Assess the morphology of the erythrocytes.
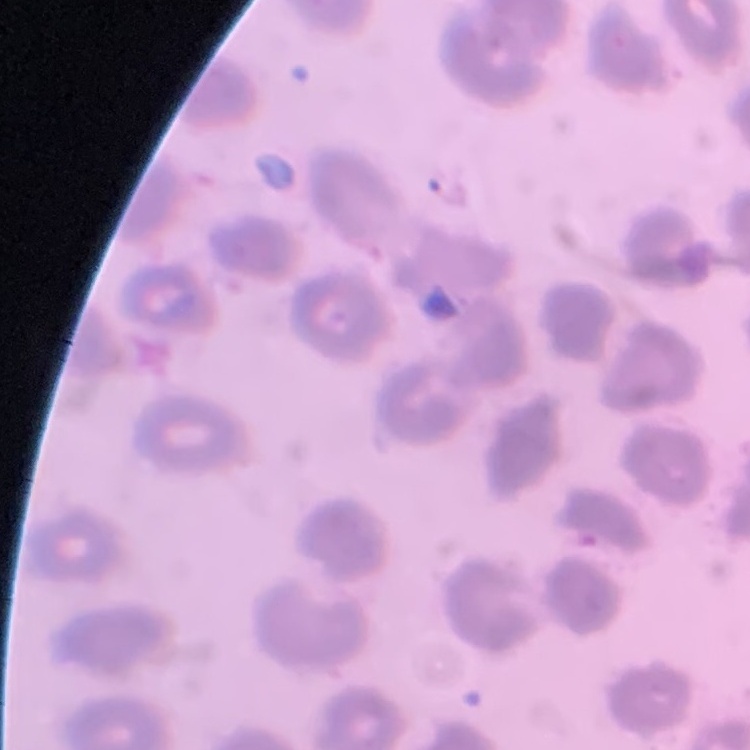
No rouleaux formation.

Stained with either Field's or Giemsa. Thin blood film. Square crop of a larger photomicrograph.